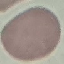

malaria status = uninfected
stain = Giemsa
preparation = thin blood smear
image type = automatically extracted cell patch, resized to 64 × 64 pixels
capture = smartphone camera at the microscope eyepiece